Outline each blood parasite and name the species.
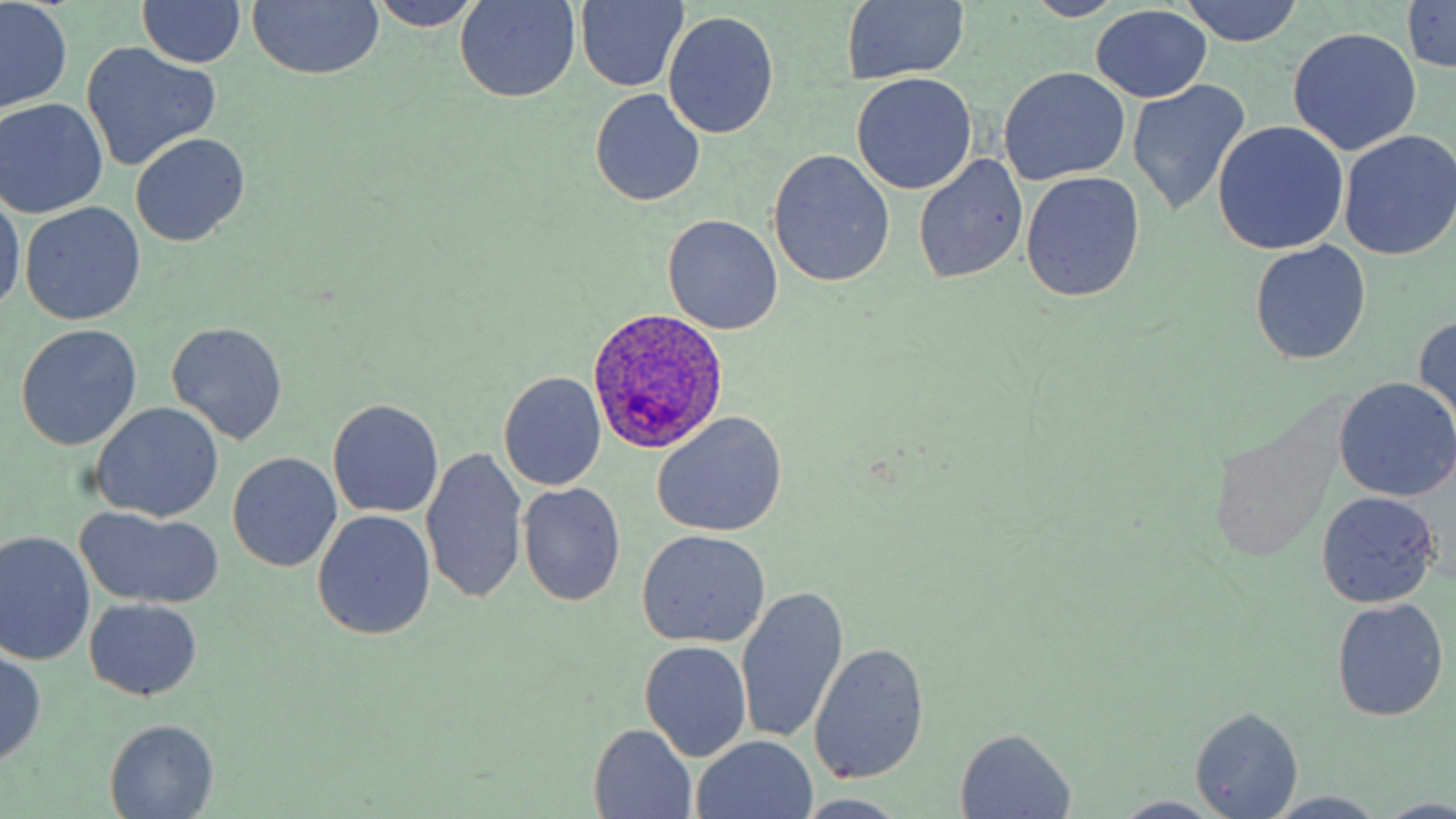
Approximate bounding boxes as (x1, y1, x2, y2) in pixels.
Plasmodium ovale-infected red blood cells: (588, 307, 727, 454).
No Plasmodium falciparum, Plasmodium malariae, Plasmodium vivax, Babesia divergens, or Trypanosoma brucei observed.

Summary:
  - Uninfected red blood cell locations: (139, 0, 245, 68), (365, 0, 487, 31), (1179, 0, 1303, 47), (248, 1, 385, 81), (454, 1, 581, 103), (572, 1, 690, 89), (840, 1, 970, 87), (1402, 1, 1456, 75), (1, 3, 72, 111), (1092, 6, 1212, 102), (663, 11, 780, 140), (1287, 27, 1421, 155), (81, 43, 221, 171), (1000, 68, 1129, 184), (852, 73, 977, 194), (1128, 80, 1250, 215), (590, 89, 705, 207), (1, 99, 107, 216), (1212, 121, 1348, 255), (1339, 131, 1455, 259), (131, 133, 248, 246), (767, 150, 896, 289), (913, 154, 1027, 285), (1022, 172, 1144, 301), (0, 188, 24, 315), (20, 203, 146, 326), (662, 214, 783, 335), (1250, 241, 1370, 363), (1414, 316, 1456, 428), (166, 321, 288, 445), (15, 325, 142, 449), (499, 372, 606, 491), (1333, 377, 1456, 501), (328, 398, 444, 519), (90, 401, 224, 522), (653, 412, 788, 539), (419, 445, 529, 606), (227, 452, 342, 573), (517, 481, 626, 607), (1316, 491, 1440, 607), (76, 508, 225, 611), (313, 512, 434, 639), (635, 530, 771, 647), (0, 531, 96, 665), (735, 584, 849, 745), (1331, 598, 1448, 722), (84, 599, 202, 701), (639, 640, 753, 762), (808, 643, 931, 786), (0, 646, 47, 765), (1189, 706, 1303, 818), (104, 719, 221, 817), (588, 725, 698, 818), (954, 728, 1077, 818), (693, 736, 816, 818), (1264, 792, 1391, 818), (796, 796, 909, 817), (1107, 796, 1228, 819), (1379, 797, 1456, 819)
  - Slide-level diagnosis: Plasmodium ovale
  - Magnification: 1000x
  - Preparation: thin blood film
  - Stain: May-Grünwald-Giemsa
  - Modality: light microscopy
  - Image size: 1456×819 pixels
  - Field of view: one of a larger specimen